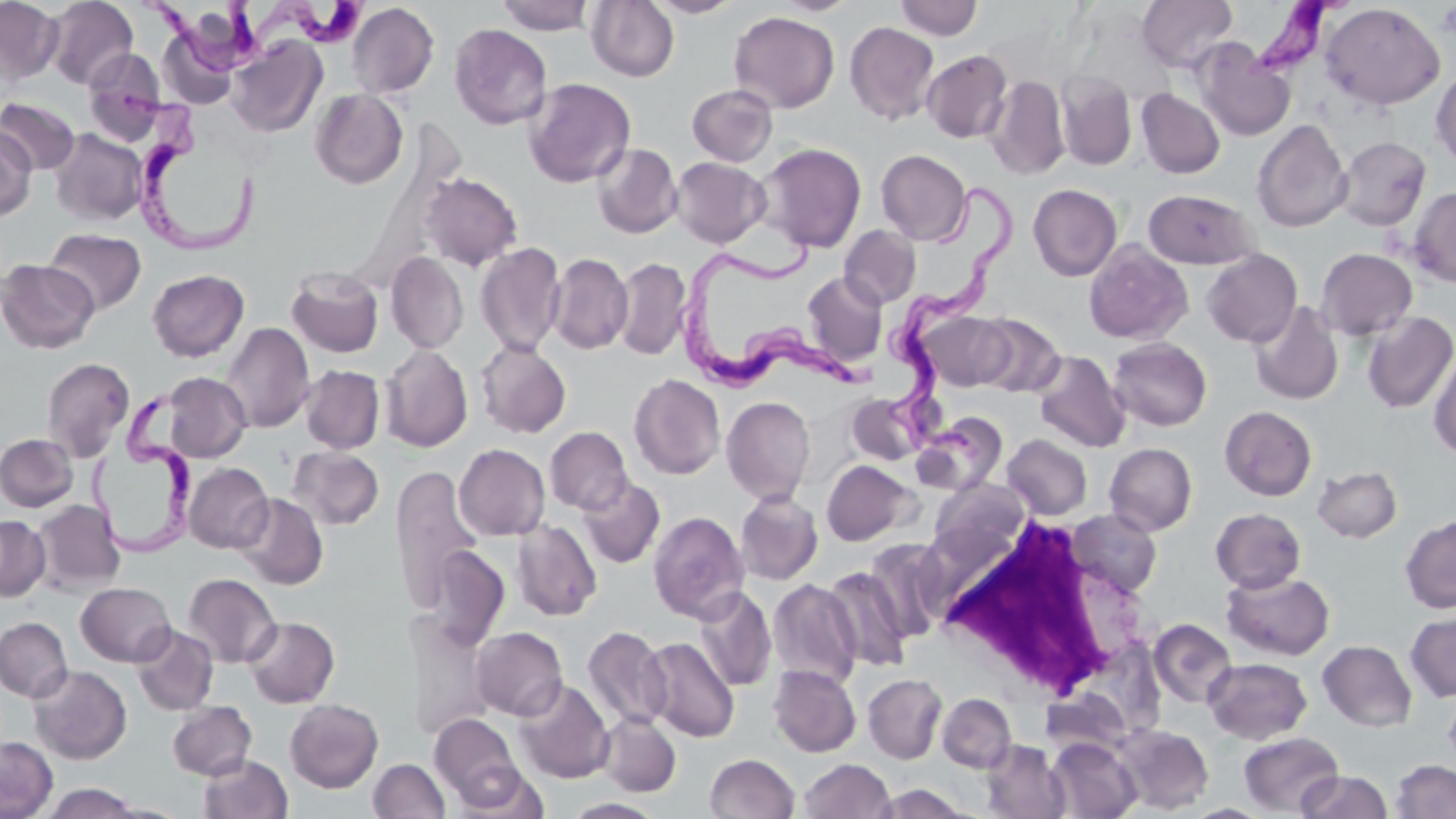
Approximate bounding boxes as (x1, y1, x2, y2) in pixels. Platelet locations: (1438, 3, 1456, 41). Trypanosoma brucei locations: (243, 0, 365, 56), (1249, 0, 1345, 77), (145, 2, 267, 81), (119, 88, 259, 262), (882, 180, 1024, 460), (666, 230, 883, 395), (93, 401, 198, 563). Uninfected red blood cell locations: (0, 0, 63, 85), (46, 0, 138, 90), (496, 0, 594, 35), (586, 0, 679, 82), (646, 0, 743, 18), (773, 0, 858, 16), (894, 0, 982, 40), (1137, 0, 1237, 73), (347, 2, 439, 98), (1320, 2, 1446, 111), (729, 11, 839, 113), (844, 22, 939, 125), (449, 24, 552, 129), (228, 36, 327, 137), (1192, 39, 1294, 141), (82, 49, 167, 142), (922, 49, 1012, 143), (1431, 66, 1456, 170), (1056, 70, 1137, 170), (985, 74, 1070, 180), (523, 78, 636, 187), (687, 84, 778, 166), (1137, 88, 1225, 179), (310, 89, 408, 189), (0, 97, 80, 176), (1252, 119, 1352, 233), (0, 127, 36, 222), (50, 129, 148, 226), (1335, 136, 1431, 231), (756, 142, 867, 253), (592, 143, 682, 239), (876, 149, 971, 245), (670, 156, 769, 247), (420, 171, 523, 271), (1028, 184, 1122, 281), (1408, 186, 1456, 287), (1143, 189, 1256, 269), (839, 225, 921, 309), (44, 228, 146, 315), (1084, 240, 1193, 345), (475, 242, 566, 356), (1201, 248, 1302, 347), (1316, 248, 1417, 340), (386, 251, 468, 354), (547, 253, 633, 354), (612, 257, 691, 361), (0, 259, 100, 354), (286, 266, 384, 358), (147, 269, 249, 362), (802, 272, 888, 365), (1249, 301, 1344, 405), (918, 310, 1012, 391), (1363, 312, 1456, 413), (972, 313, 1065, 398), (221, 322, 314, 433), (1108, 337, 1212, 431), (475, 339, 571, 438), (380, 344, 472, 452), (1429, 350, 1456, 460), (1032, 351, 1130, 453), (41, 358, 134, 461), (301, 364, 385, 454), (162, 373, 251, 462), (629, 374, 725, 479), (847, 392, 927, 466), (721, 396, 815, 505), (1220, 405, 1317, 501), (913, 412, 1008, 496), (545, 426, 632, 515), (1, 433, 78, 512), (1003, 434, 1092, 520), (1104, 443, 1197, 536), (453, 444, 550, 541), (287, 446, 384, 530), (821, 460, 916, 545), (185, 462, 274, 553), (389, 465, 483, 612), (1313, 466, 1402, 542), (577, 476, 666, 569), (929, 480, 1030, 562), (735, 490, 823, 585), (234, 493, 328, 590), (31, 500, 126, 595), (1210, 508, 1306, 593), (1068, 509, 1162, 596), (648, 510, 749, 623), (0, 515, 50, 602), (1400, 515, 1456, 613), (512, 519, 602, 621), (864, 538, 950, 641), (425, 544, 510, 650), (822, 566, 912, 671), (1221, 570, 1335, 660), (183, 572, 282, 669), (767, 579, 861, 689), (76, 582, 175, 666), (693, 587, 777, 691), (1405, 612, 1456, 702), (407, 615, 493, 741), (244, 616, 339, 708), (0, 617, 73, 702), (1148, 618, 1237, 708), (131, 624, 218, 716), (582, 625, 671, 731), (471, 627, 568, 720), (641, 636, 739, 742), (1317, 640, 1417, 731), (1204, 657, 1312, 744), (29, 665, 131, 764), (768, 665, 861, 757), (863, 673, 947, 764), (514, 679, 614, 783), (1444, 687, 1456, 776), (1039, 690, 1132, 758), (937, 693, 1016, 772), (285, 698, 383, 793), (167, 701, 256, 780), (598, 712, 681, 796), (429, 713, 523, 805), (1114, 724, 1214, 813), (1239, 731, 1344, 817), (0, 736, 58, 819), (1047, 738, 1142, 819), (982, 740, 1070, 819), (704, 752, 799, 819), (198, 754, 293, 819), (368, 758, 450, 819), (799, 758, 896, 818), (1390, 760, 1456, 818), (451, 764, 548, 818), (1297, 770, 1392, 818), (40, 783, 144, 818), (873, 784, 974, 818), (563, 798, 667, 818), (1185, 803, 1270, 818). White blood cell locations: (927, 515, 1148, 706). Slide-level diagnosis: Trypanosoma brucei. Single field of view. May-Grünwald-Giemsa stain. Optical microscopy. Image is 1456×819 pixels. Thin blood smear. Captured at 1000x magnification.